Outline each blood parasite and name the species.
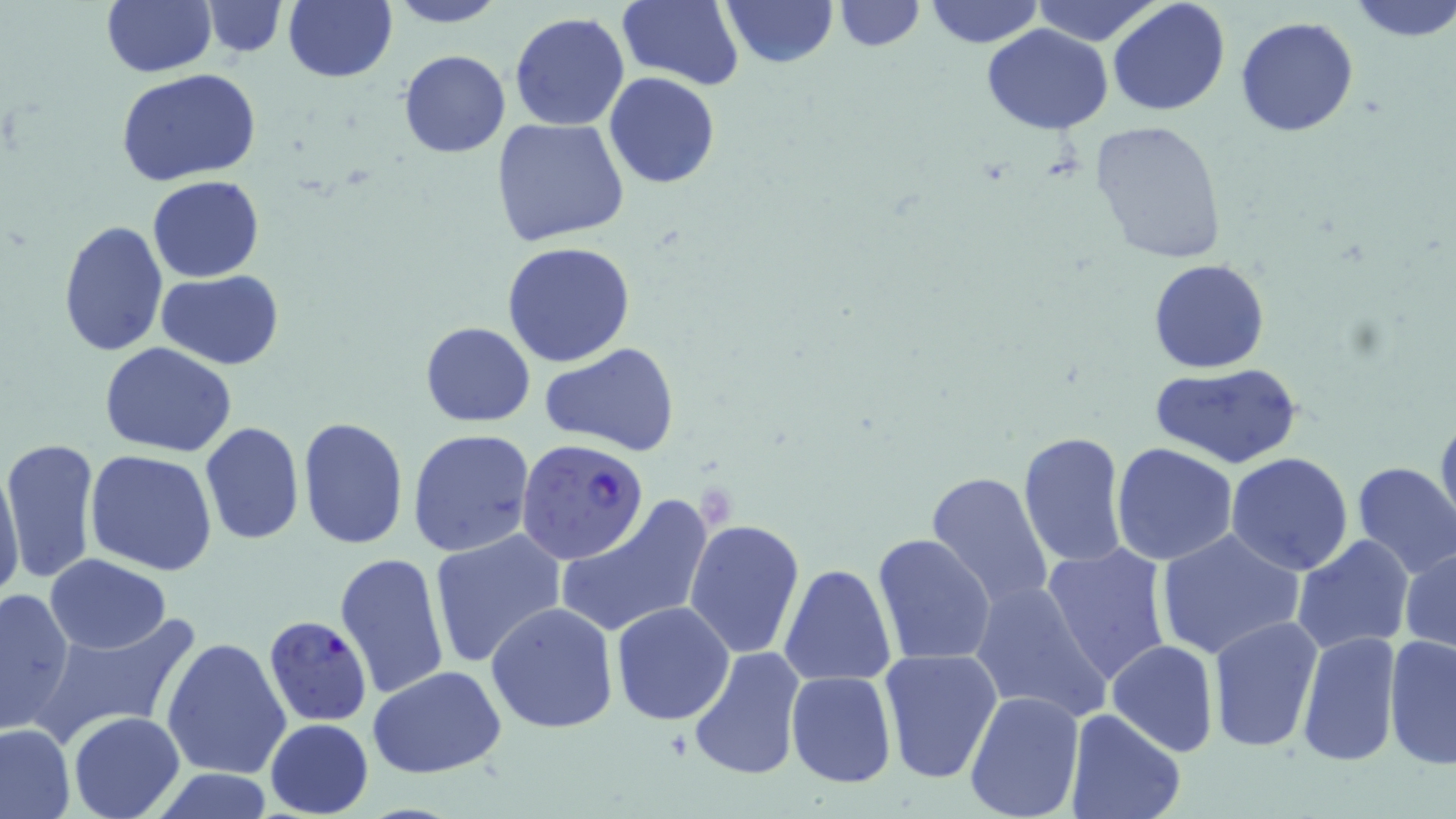
Approximate bounding boxes as (x1, y1, x2, y2) in pixels.
Plasmodium falciparum-infected red blood cells: (516, 438, 649, 565), (269, 619, 367, 727).
No Plasmodium ovale, Plasmodium malariae, Plasmodium vivax, Babesia divergens, or Trypanosoma brucei observed.

Summary:
  - Uninfected red blood cell locations: (283, 0, 397, 83), (616, 0, 743, 90), (719, 0, 837, 68), (922, 0, 1044, 48), (1032, 0, 1164, 47), (1346, 0, 1456, 41), (102, 1, 215, 76), (385, 1, 508, 28), (833, 1, 923, 52), (1107, 1, 1230, 117), (201, 2, 287, 57), (509, 11, 631, 132), (1235, 15, 1360, 137), (982, 24, 1113, 133), (397, 49, 512, 158), (118, 69, 261, 186), (604, 73, 721, 189), (492, 117, 630, 246), (1087, 119, 1228, 264), (146, 175, 265, 282), (58, 218, 169, 360), (502, 241, 635, 368), (1149, 259, 1270, 373), (156, 269, 285, 370), (420, 320, 536, 427), (99, 343, 240, 457), (538, 343, 681, 456), (1151, 362, 1302, 469), (1435, 411, 1456, 534), (297, 416, 409, 552), (200, 422, 304, 546), (406, 430, 535, 560), (1017, 431, 1128, 571), (2, 435, 100, 586), (1112, 444, 1238, 566), (85, 450, 219, 577), (1225, 452, 1354, 575), (1, 458, 25, 608), (1351, 461, 1456, 578), (927, 470, 1054, 613), (554, 495, 714, 640), (684, 519, 805, 659), (1154, 527, 1306, 662), (428, 529, 567, 668), (872, 533, 997, 667), (1292, 535, 1417, 657), (1040, 544, 1172, 691), (1402, 544, 1456, 656), (334, 551, 450, 701), (45, 554, 172, 654), (779, 563, 897, 688), (969, 578, 1111, 723), (0, 586, 76, 735), (485, 601, 619, 736), (611, 602, 734, 725), (31, 615, 198, 746), (1207, 616, 1325, 755), (1295, 630, 1399, 766), (1384, 635, 1455, 771), (161, 637, 291, 780), (1106, 639, 1219, 758), (688, 647, 804, 782), (877, 648, 1002, 781), (367, 667, 509, 780), (786, 672, 897, 789), (963, 690, 1087, 819), (1062, 710, 1186, 819), (69, 712, 185, 819), (265, 718, 373, 817), (0, 723, 75, 818)
  - Slide-level diagnosis: Plasmodium falciparum
  - Modality: light microscopy
  - Magnification: 1000x
  - Preparation: thin blood smear
  - Image size: 1456×819 pixels
  - Stain: May-Grünwald-Giemsa
  - Field of view: single